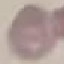

result: no malaria parasites seen
stain: Giemsa
image_type: cell patch, automatically extracted from a larger field of view and resized to 64 × 64 pixels
capture: smartphone through the microscope eyepiece
preparation: thin blood smear